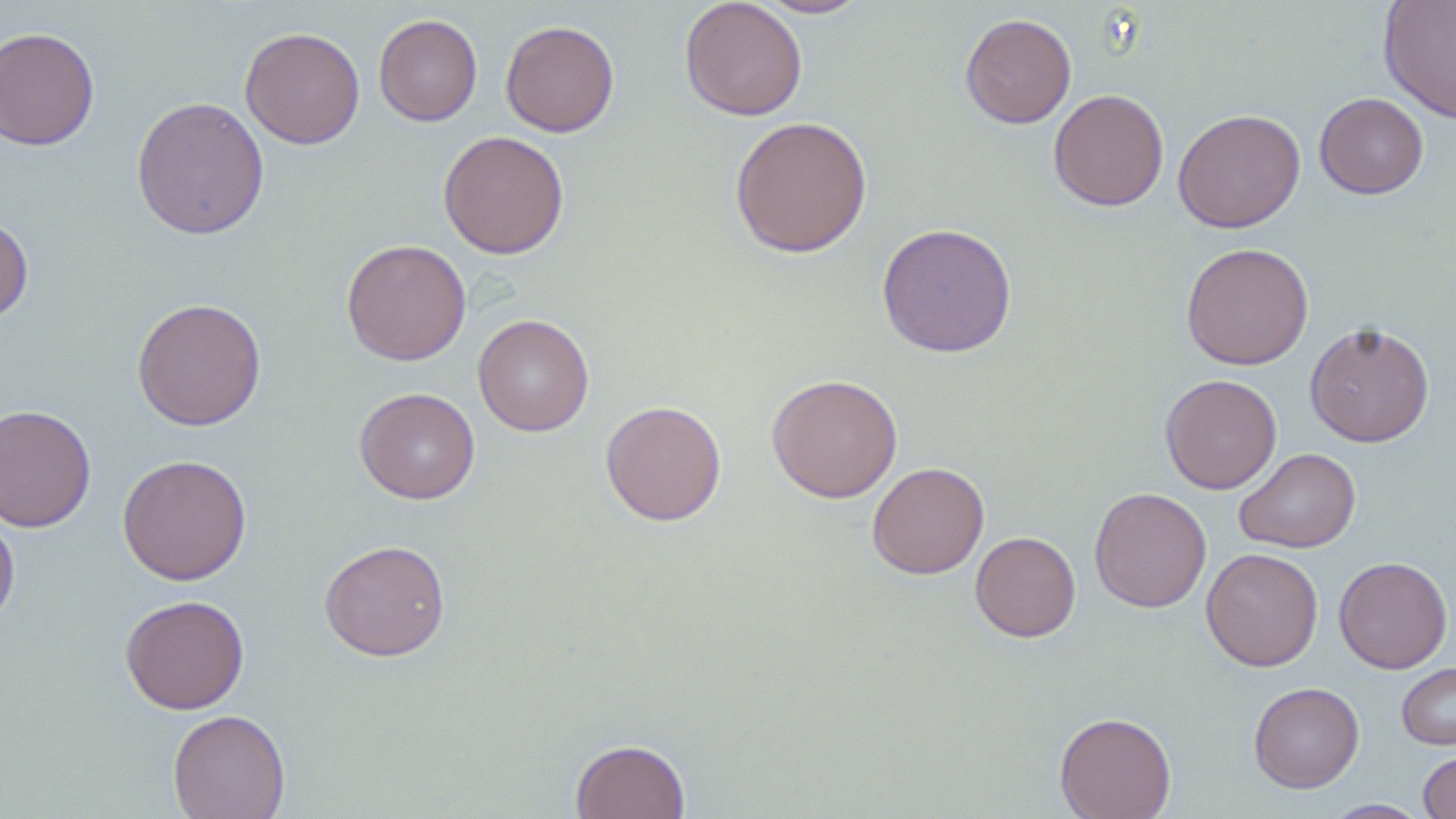
Approximate bounding boxes as (x1, y1, x2, y2) in pixels. Uninfected red blood cell locations: (679, 0, 808, 121), (754, 0, 869, 18), (1379, 1, 1456, 125), (959, 12, 1077, 128), (373, 13, 483, 126), (500, 20, 620, 137), (0, 26, 100, 152), (240, 26, 365, 150), (1048, 88, 1169, 211), (1314, 92, 1430, 199), (130, 96, 270, 240), (1172, 108, 1305, 233), (729, 115, 873, 258), (438, 130, 569, 259), (0, 215, 34, 325), (876, 222, 1017, 358), (341, 239, 471, 365), (1180, 242, 1314, 370), (131, 297, 267, 431), (473, 314, 594, 436), (1304, 321, 1435, 447), (766, 373, 903, 503), (1159, 373, 1282, 494), (355, 387, 480, 504), (600, 400, 727, 526), (0, 404, 97, 532), (1233, 447, 1361, 553), (117, 453, 252, 585), (867, 461, 989, 579), (1089, 486, 1212, 613), (0, 509, 20, 635), (970, 531, 1081, 642), (319, 539, 451, 661), (1201, 547, 1323, 672), (1333, 556, 1452, 673), (120, 594, 250, 714), (1397, 662, 1456, 750), (1248, 681, 1364, 793), (167, 709, 291, 819), (1054, 711, 1177, 819), (570, 738, 690, 819), (1418, 750, 1456, 818), (1323, 799, 1431, 818). Slide-level diagnosis: no evidence of blood parasites. Thin blood film. Image is 1456×819 pixels. May-Grünwald-Giemsa stain. Light microscopy. 1000x magnification. Single field of view.